Point out each Plasmodium parasite.
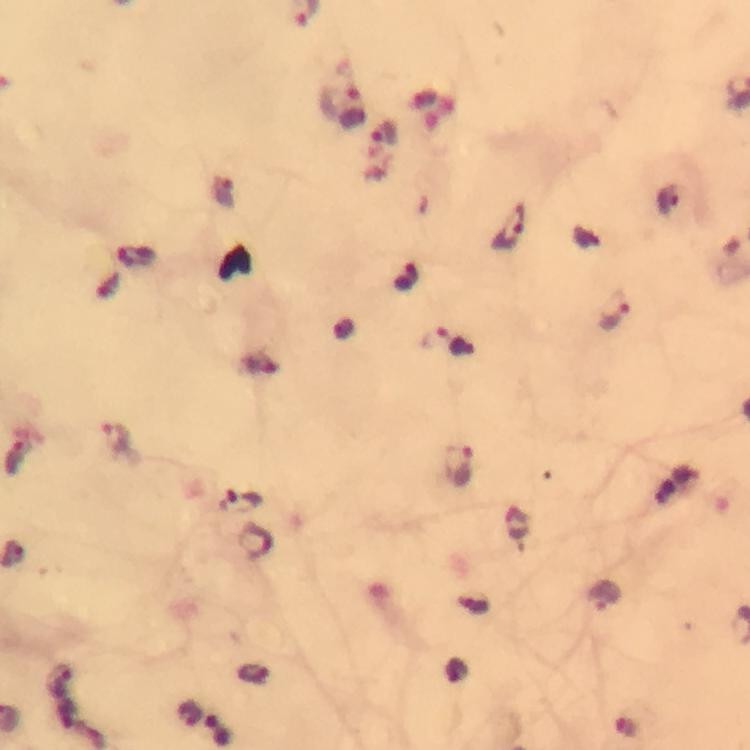
Approximate centers as {x, y} in pixels.
Plasmodium parasites: {353, 108}, {386, 135}, {509, 229}, {615, 311}, {453, 343}, {118, 440}, {15, 457}, {457, 466}, {241, 504}, {257, 542}, {606, 596}.

From a diagnostic examination for malaria. Smartphone photograph taken through a microscope. At 100x magnification. Immersion oil applied. Image is 750×750 pixels. Cropped region of a single field of view. Thick blood film. Giemsa-stained preparation.